Assess this cell for malaria.
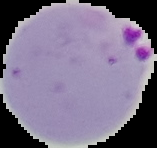
It is parasitized.

Segmented cell region on a black background. Image is 157×148 pixels. From a thin blood film.